Identify the cell.
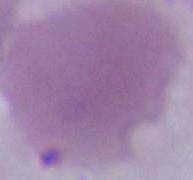

An erythrocyte.

magnification: 1000x
modality: micrograph